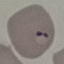

Summary:
  - Result: malaria parasites detected
  - Stain: Giemsa
  - Capture: smartphone camera at the microscope eyepiece
  - Image type: automatically extracted cell patch, resized to 64 × 64 pixels
  - Preparation: thin blood smear